Point out each Plasmodium parasite.
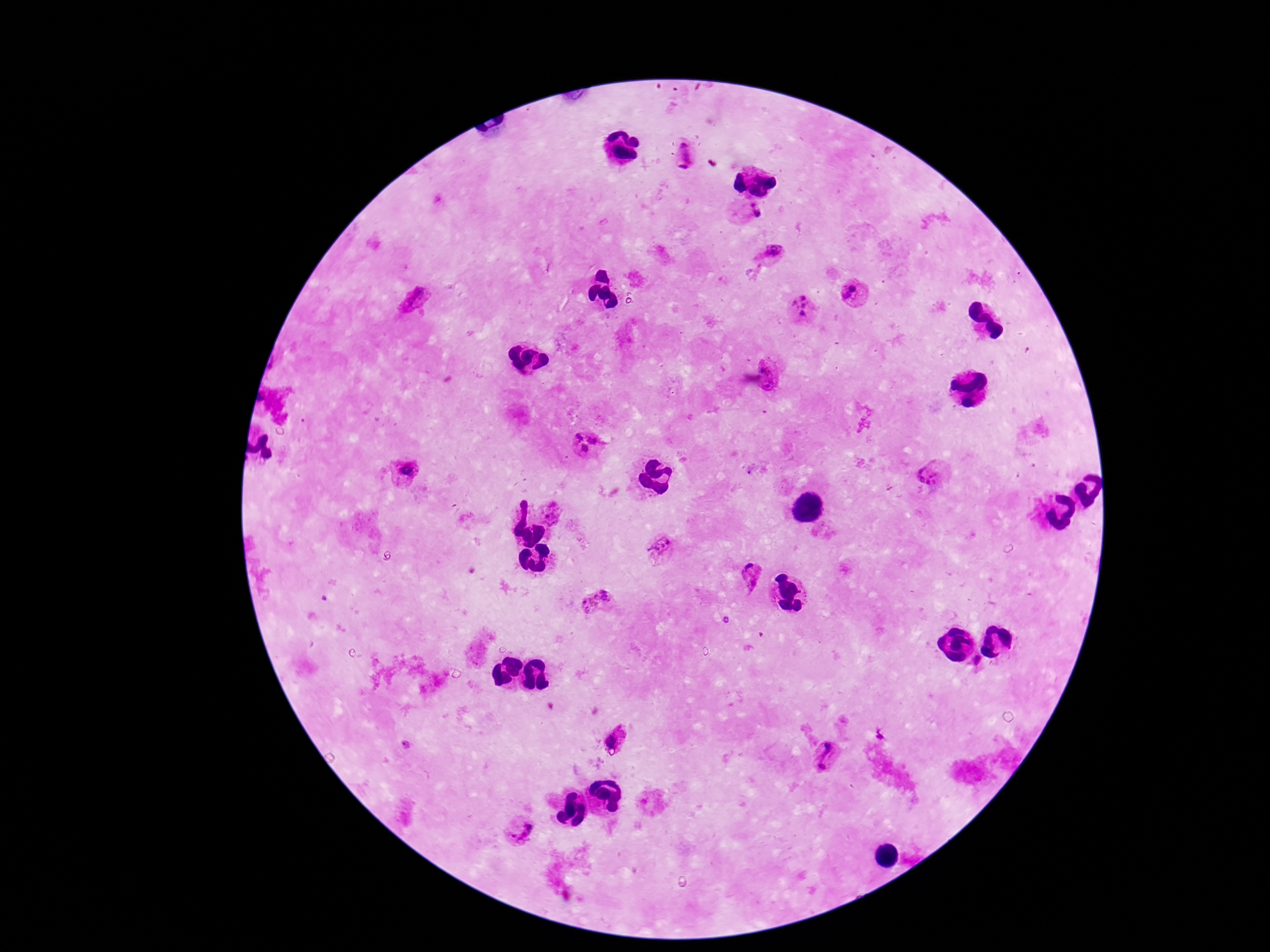
Approximate centers as {x, y} in pixels.
Plasmodium parasites: {682, 144}, {688, 154}, {682, 167}, {750, 214}, {771, 251}, {852, 289}, {846, 294}, {803, 298}, {415, 300}, {795, 303}, {803, 306}, {802, 314}, {766, 369}, {771, 385}, {579, 437}, {592, 439}, {585, 448}, {409, 468}, {927, 474}, {553, 513}, {663, 547}, {752, 575}, {599, 602}, {615, 735}, {828, 747}, {823, 764}, {521, 831}.

Summary:
  - Patient malaria status: positive
  - Image size: 1270×952 pixels
  - Field of view: one from this slide
  - Capture: smartphone camera through the microscope eyepiece
  - Magnification: 100x
  - Stain: Giemsa
  - Preparation: thick blood film